Give the position of every Plasmodium parasite.
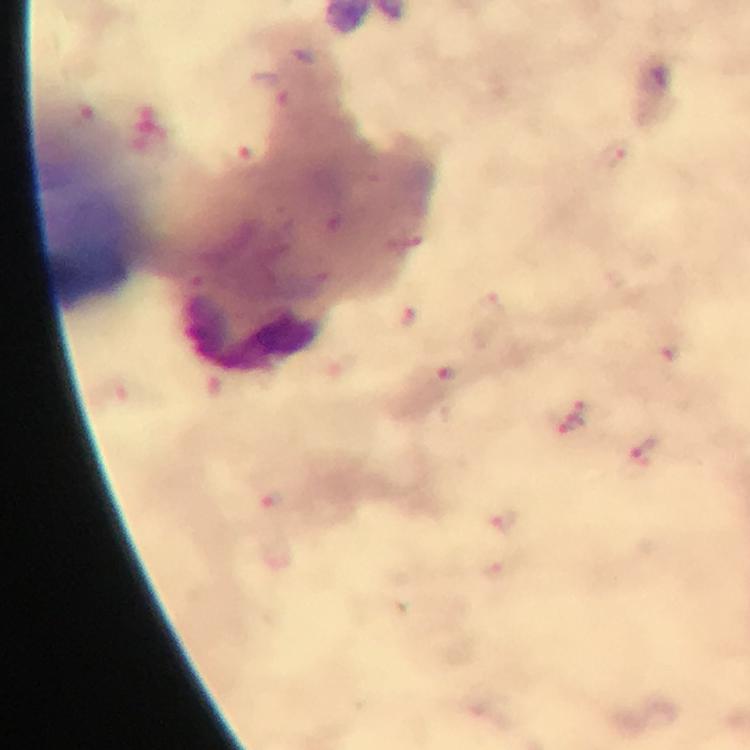

Approximate centers as {x, y} in pixels.
Plasmodium parasites: {617, 154}, {408, 319}, {449, 375}, {576, 418}, {504, 523}.

A crop from one field of view. Giemsa stain. Immersion oil was used. Thick smear. At 100x magnification. Photographed through the microscope with a smartphone camera. From a diagnostic examination for malaria. Image is 750×750 pixels.